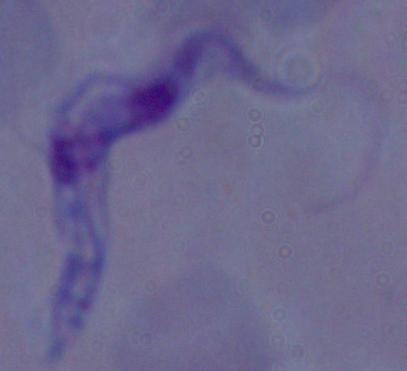

Summary:
  - Magnification: 1000x
  - Modality: micrograph
  - Identification: trypanosome